Classify this cell by malaria status.
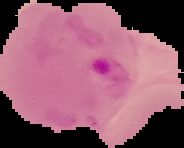

Parasitized.

Summary:
  - Image size: 184×148 pixels
  - Preparation: thin blood smear
  - Image type: segmented cell region on a black background